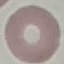

{
  "malaria_status": "uninfected",
  "stain": "Giemsa",
  "image_type": "cell patch, automatically extracted from a larger field of view and resized to 64 × 64 pixels",
  "capture": "smartphone camera at the microscope eyepiece",
  "preparation": "thin smear"
}